Name the cell type shown.
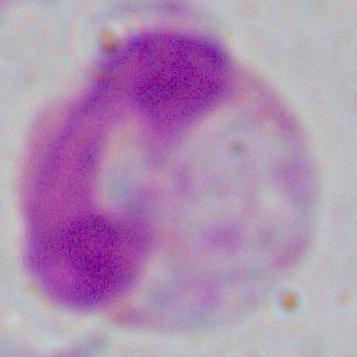

This is a leukocyte.

modality = micrograph
magnification = 1000x